State which parasite is depicted.
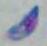

This is Toxoplasma gondii.

1000x magnification. Micrograph.